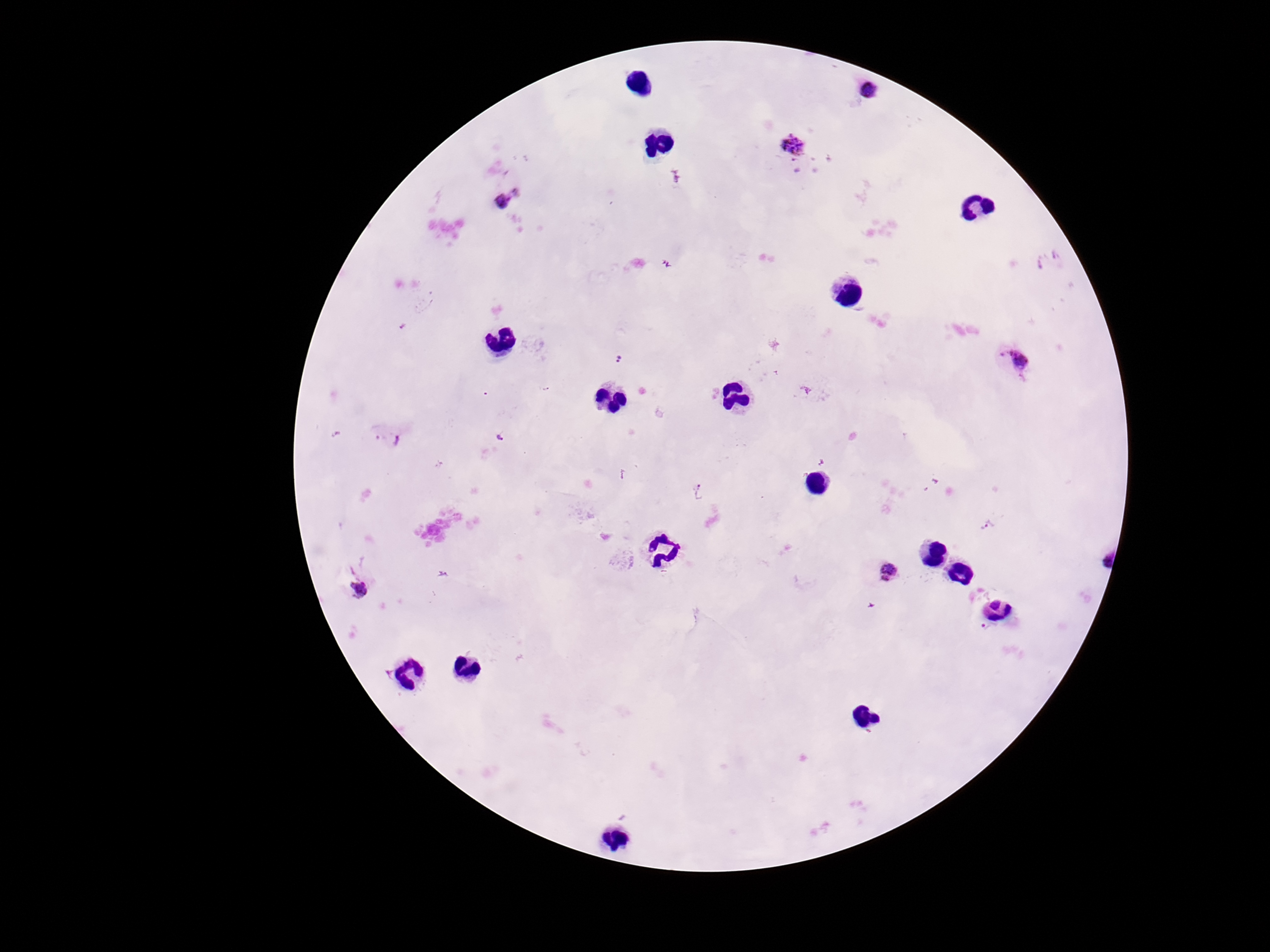

Approximate centers as (x, y) in pixels.
Summary:
  - Plasmodium parasite locations: (870, 92), (792, 148), (507, 198), (619, 360), (1014, 360), (546, 387), (498, 436), (388, 439), (701, 492), (989, 525), (1105, 554), (886, 570), (361, 589), (987, 628)
  - Field of view: one from this slide
  - Magnification: 100x
  - Patient malaria status: positive
  - Capture: smartphone camera through the microscope eyepiece
  - Stain: Giemsa
  - Preparation: thick blood film
  - Image size: 1270×952 pixels